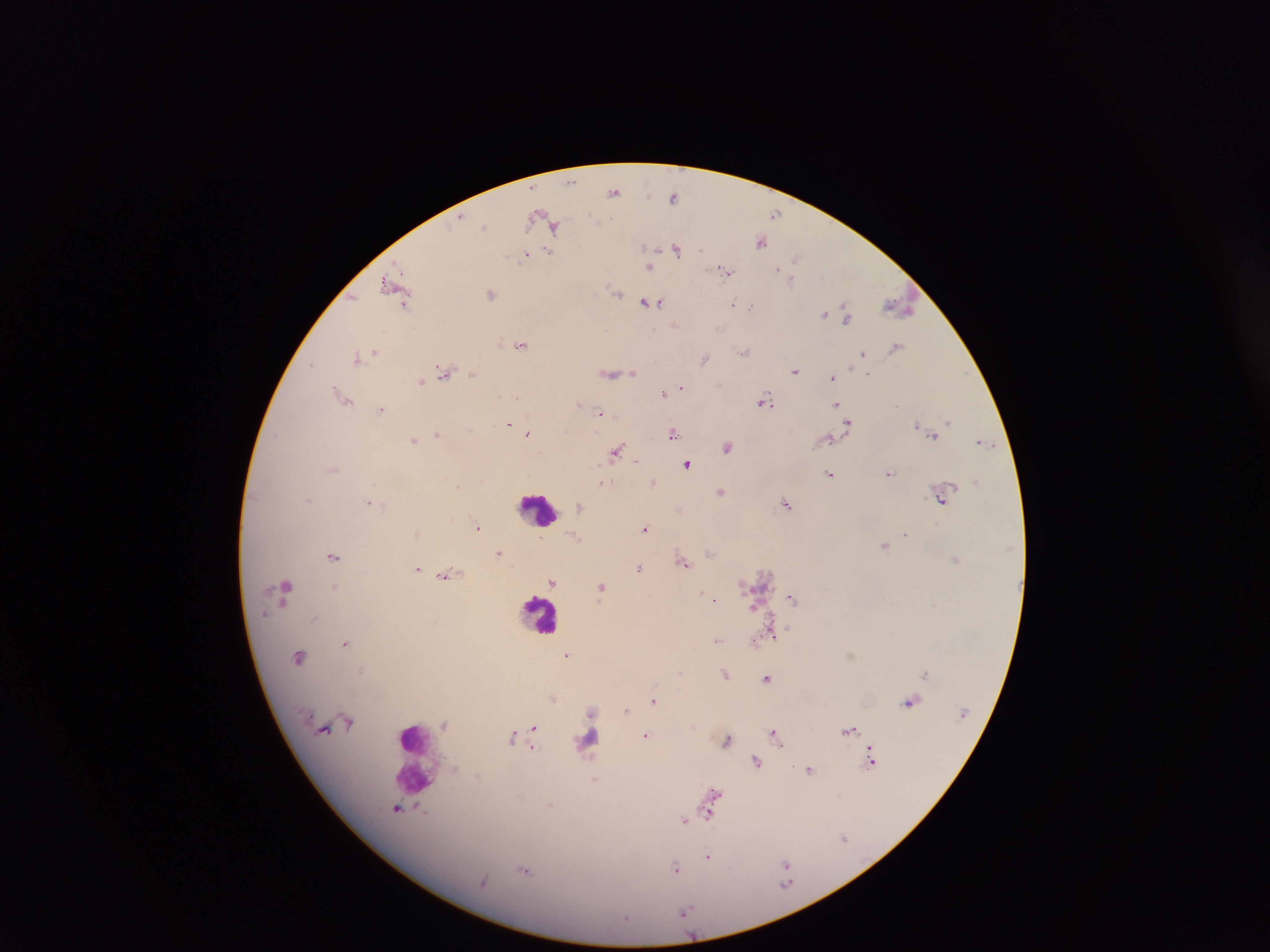 Approximate centers as {x, y} in pixels. Leukocyte locations: {537, 509}, {540, 613}, {592, 738}, {412, 755}. Malaria parasite locations: {572, 181}, {614, 192}, {673, 196}, {775, 213}, {459, 218}, {484, 225}, {555, 226}, {760, 241}, {676, 249}, {700, 249}, {549, 251}, {525, 254}, {795, 257}, {650, 268}, {778, 269}, {725, 271}, {792, 281}, {388, 284}, {616, 293}, {490, 294}, {645, 302}, {657, 302}, {405, 303}, {733, 305}, {752, 305}, {899, 306}, {823, 313}, {848, 316}, {674, 325}, {720, 328}, {520, 345}, {896, 347}, {744, 351}, {374, 352}, {863, 353}, {357, 357}, {705, 359}, {312, 365}, {443, 371}, {794, 371}, {624, 373}, {633, 373}, {472, 374}, {612, 374}, {867, 374}, {833, 378}, {421, 381}, {681, 386}, {663, 394}, {342, 396}, {517, 397}, {764, 400}, {579, 403}, {837, 403}, {381, 410}, {600, 413}, {949, 422}, {848, 423}, {509, 425}, {918, 425}, {528, 433}, {673, 433}, {437, 434}, {934, 435}, {829, 439}, {413, 440}, {982, 442}, {728, 447}, {617, 451}, {636, 460}, {687, 464}, {889, 473}, {830, 474}, {653, 481}, {602, 482}, {721, 492}, {308, 499}, {942, 500}, {368, 503}, {786, 504}, {580, 506}, {680, 508}, {477, 526}, {645, 529}, {906, 534}, {885, 545}, {710, 551}, {499, 553}, {332, 557}, {954, 558}, {684, 562}, {417, 568}, {639, 568}, {448, 573}, {552, 582}, {335, 586}, {602, 587}, {285, 590}, {702, 593}, {792, 597}, {714, 599}, {935, 604}, {263, 614}, {314, 619}, {772, 634}, {717, 640}, {345, 643}, {567, 655}, {299, 657}, {680, 672}, {724, 673}, {926, 673}, {767, 678}, {553, 699}, {653, 700}, {909, 702}, {626, 710}, {348, 722}, {534, 727}, {849, 730}, {775, 734}, {645, 735}, {512, 737}, {727, 740}, {533, 747}, {871, 758}, {756, 761}, {809, 770}, {596, 779}, {710, 799}, {396, 807}, {420, 808}, {709, 811}, {684, 820}, {844, 838}, {708, 856}, {786, 864}, {675, 869}, {525, 870}, {684, 912}, {626, 918}. Single field of view. Sample from Ghana. Image is 1270×952 pixels. Thick blood film. Photographed through a microscope with a mobile-phone camera.